Report the malaria status of this cell.
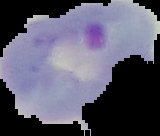
Parasitized.

Summary:
  - Image size: 160×136 pixels
  - Preparation: thin blood film
  - Image type: segmented cell region with the area outside set to black